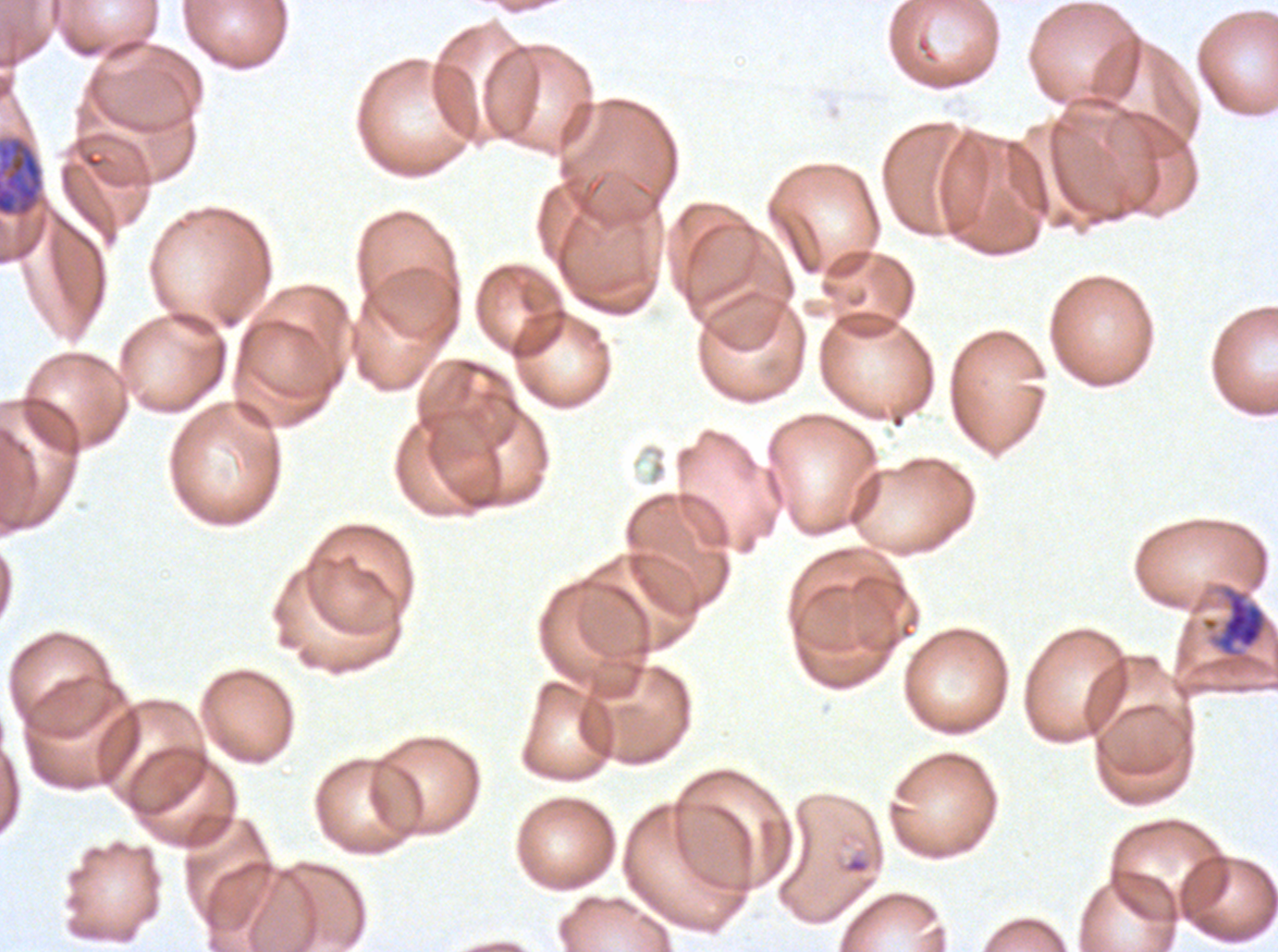
{
  "early_schizont_locations": "approximate bounding boxes as [x1, y1, x2, y2] in pixels: [0, 138, 43, 216], [1207, 583, 1270, 667]",
  "life_cycle_stages_observed": "late-ring/early-trophozoite, early schizont",
  "specimen": "P. falciparum cultured ex vivo for 24 to 48 hours, from a patient in The Gambia",
  "preparation": "thin blood film",
  "field_of_view": "one sub-image of a larger composite",
  "image_size": "1278×952 pixels",
  "late_ring_early_trophozoite_locations": "approximate bounding boxes as [x1, y1, x2, y2] in pixels: [842, 852, 871, 875]",
  "stain": "Giemsa"
}